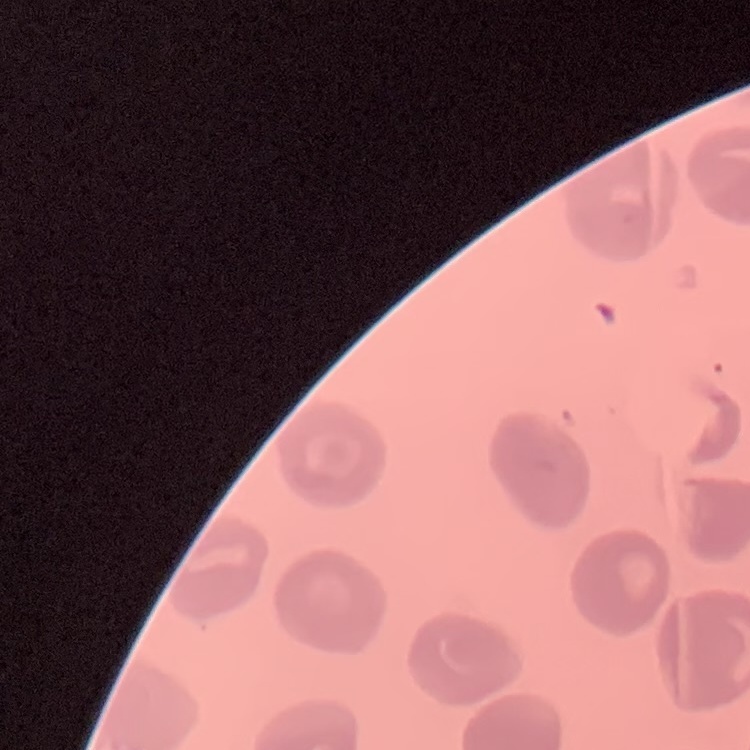

{
  "red_blood_cell_morphology": "no rouleaux formation",
  "stain": "Field's or Giemsa",
  "image_type": "one tile cut from a larger photomicrograph",
  "preparation": "thin blood film"
}